Assess this cell for malaria.
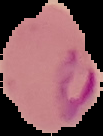
Parasitized.

image size = 103×136 pixels
preparation = thin blood film
image type = cell region segmented out of the field of view; surrounding area masked to black